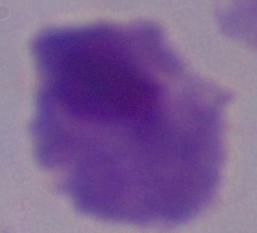
Micrograph. Captured at 1000x magnification. A trichomonad is seen.